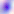
Photomicrograph. 400x magnification. Toxoplasma gondii is shown.